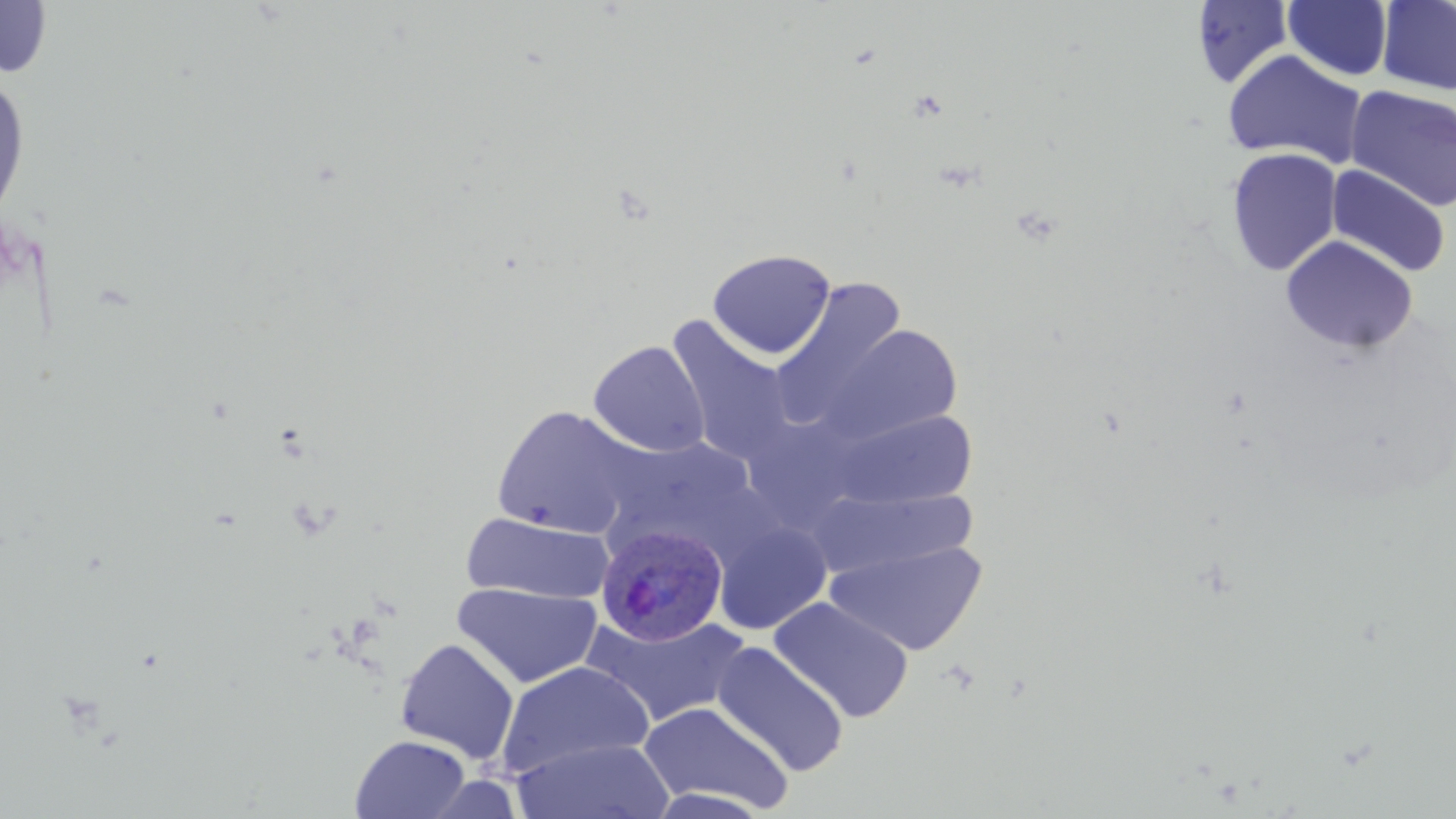
Summary:
  - Coordinate format: approximate bounding boxes as (x1, y1, x2, y2) in pixels
  - Plasmodium ovale-infected red blood cell locations: (595, 524, 728, 646)
  - Uninfected red blood cell locations: (1283, 0, 1393, 81), (1377, 0, 1456, 97), (0, 1, 54, 81), (1191, 1, 1294, 89), (1222, 49, 1369, 169), (0, 70, 31, 229), (1344, 86, 1456, 212), (1226, 147, 1342, 276), (1326, 165, 1451, 278), (1281, 236, 1418, 353), (706, 249, 836, 359), (770, 279, 908, 429), (665, 318, 796, 467), (825, 324, 963, 445), (588, 340, 710, 458), (491, 405, 640, 539), (830, 408, 978, 510), (601, 436, 764, 526), (810, 487, 981, 579), (461, 511, 614, 605), (714, 520, 831, 634), (825, 539, 987, 656), (452, 581, 604, 688), (769, 597, 914, 724), (583, 613, 750, 728), (395, 638, 519, 763), (712, 642, 850, 777), (495, 661, 654, 780), (638, 701, 793, 815), (350, 734, 471, 819), (511, 737, 675, 819), (643, 788, 778, 819)
  - Slide-level diagnosis: Plasmodium ovale
  - Preparation: thin blood film
  - Image size: 1456×819 pixels
  - Field of view: single
  - Stain: May-Grünwald-Giemsa
  - Modality: optical microscopy
  - Magnification: 1000x